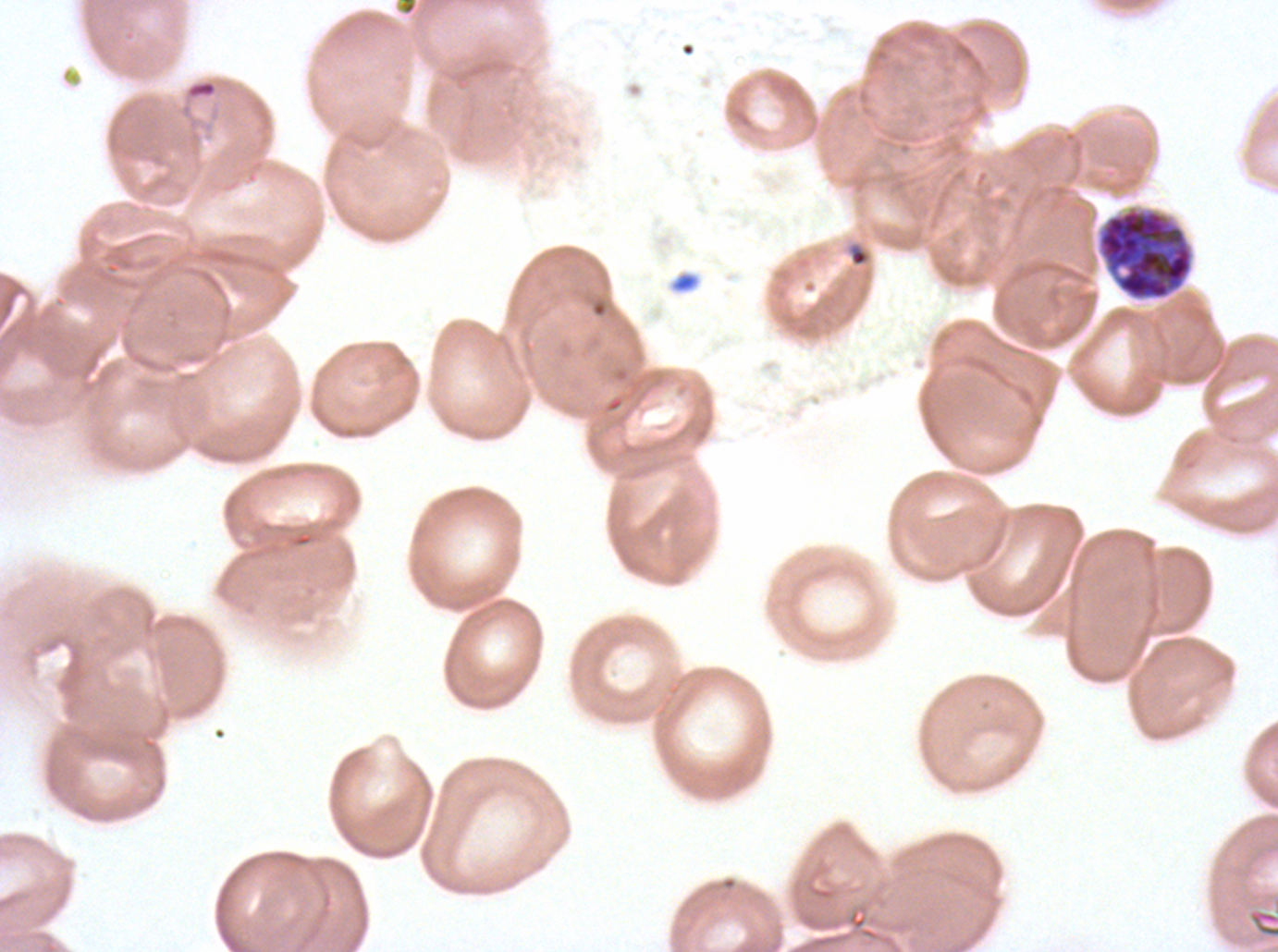
Approximate bounding boxes as [x1, y1, x2, y2] in pixels.
Summary:
  - Early schizont locations: [1097, 207, 1194, 300]
  - Ring locations: [178, 78, 231, 153], [847, 242, 871, 268]
  - Stain: Giemsa
  - Preparation: thin blood film
  - Field of view: one sub-image of a larger composite
  - Specimen: Plasmodium falciparum from a patient in The Gambia, cultured ex vivo for 24 to 48 hours
  - Life-cycle stages observed: ring, early schizont
  - Image size: 1278×952 pixels